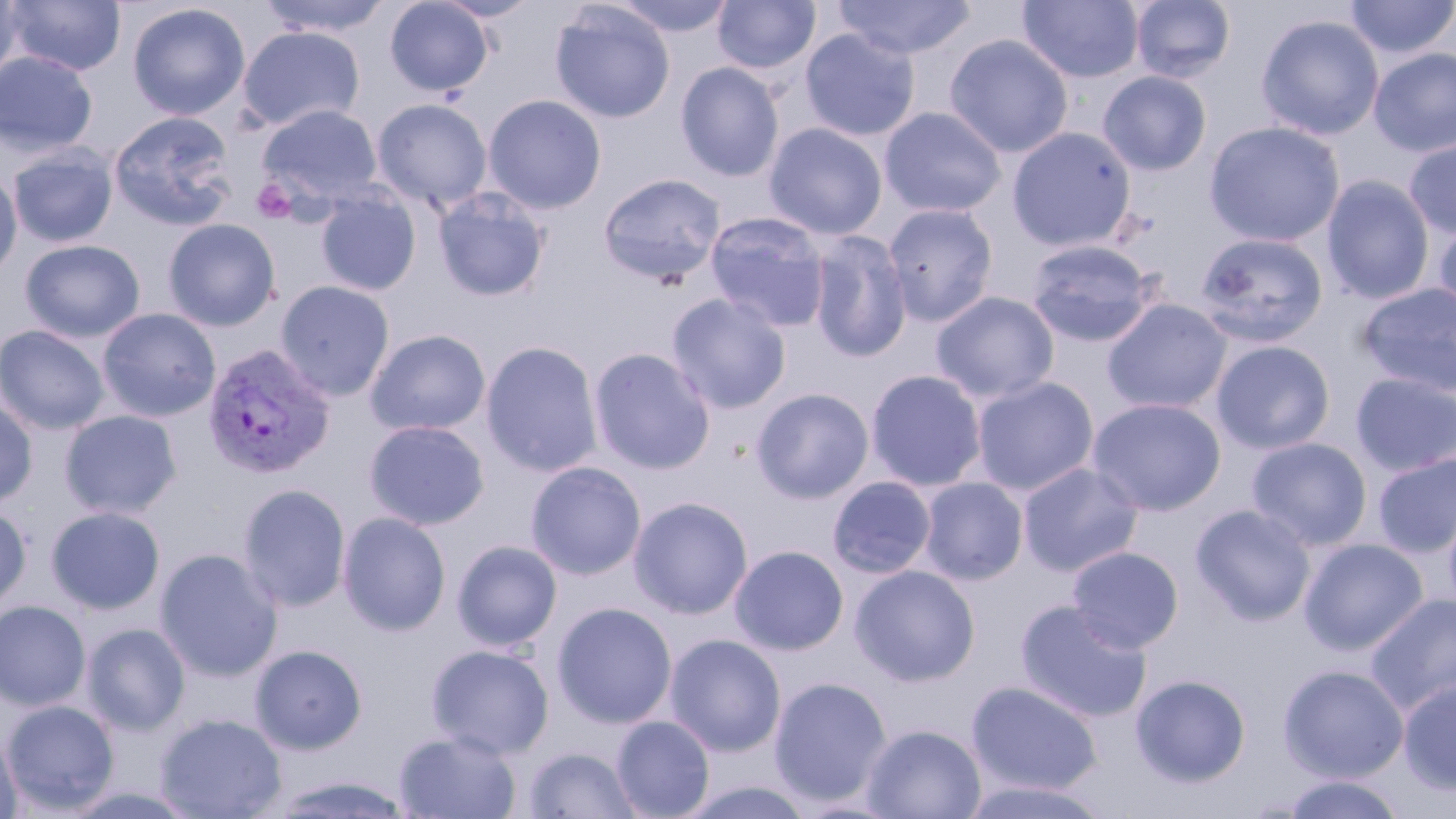

Approximate bounding boxes as (x1, y1, x2, y2) in pixels. Plasmodium vivax-infected red blood cell locations: (202, 344, 335, 478). Uninfected red blood cell locations: (0, 0, 24, 89), (4, 0, 126, 77), (256, 0, 394, 37), (384, 0, 494, 97), (432, 0, 542, 21), (611, 0, 735, 37), (712, 0, 821, 75), (829, 0, 977, 61), (1130, 0, 1235, 84), (1343, 0, 1456, 60), (1017, 1, 1145, 84), (126, 3, 250, 121), (550, 3, 675, 124), (1255, 14, 1385, 140), (238, 26, 365, 132), (799, 27, 921, 141), (944, 34, 1073, 158), (1368, 47, 1456, 157), (0, 51, 98, 158), (676, 62, 785, 182), (1097, 70, 1212, 176), (483, 94, 607, 214), (371, 98, 493, 212), (258, 104, 383, 207), (879, 106, 1007, 218), (108, 111, 237, 231), (1204, 121, 1345, 247), (764, 122, 887, 240), (1008, 127, 1136, 251), (1403, 137, 1456, 239), (7, 146, 117, 248), (0, 166, 23, 284), (597, 172, 726, 287), (1322, 174, 1435, 305), (432, 189, 551, 302), (316, 191, 421, 296), (882, 203, 999, 326), (705, 213, 832, 332), (1432, 215, 1456, 327), (163, 218, 281, 331), (808, 231, 913, 362), (1195, 232, 1328, 347), (19, 239, 145, 342), (1024, 239, 1159, 347), (275, 280, 395, 400), (1358, 282, 1456, 398), (931, 291, 1060, 403), (667, 293, 792, 414), (1102, 299, 1232, 413), (97, 308, 221, 422), (0, 324, 110, 435), (365, 329, 491, 436), (1212, 339, 1336, 454), (481, 341, 603, 477), (588, 347, 716, 475), (866, 369, 988, 492), (1351, 372, 1456, 475), (971, 376, 1099, 495), (751, 387, 875, 504), (0, 397, 38, 509), (1088, 397, 1226, 515), (60, 409, 182, 519), (363, 420, 490, 530), (354, 423, 472, 632), (1246, 437, 1372, 551), (1373, 452, 1456, 557), (525, 461, 646, 580), (1018, 462, 1143, 576), (827, 475, 937, 579), (918, 477, 1028, 585), (238, 483, 352, 612), (629, 496, 753, 619), (0, 503, 31, 612), (1190, 504, 1316, 626), (46, 506, 166, 615), (337, 512, 451, 635), (1299, 538, 1428, 655), (452, 540, 562, 650), (729, 545, 849, 655), (1067, 546, 1184, 653), (154, 548, 283, 681), (850, 565, 980, 687), (1364, 592, 1456, 717), (1015, 599, 1152, 723), (0, 601, 91, 711), (552, 602, 677, 729), (82, 623, 191, 735), (665, 633, 787, 757), (249, 644, 368, 754), (426, 644, 554, 758), (1277, 663, 1410, 782), (1130, 674, 1252, 787), (769, 677, 892, 806), (1398, 677, 1456, 796), (966, 681, 1103, 795), (2, 699, 120, 814), (155, 713, 287, 819), (611, 716, 715, 819), (861, 724, 986, 819), (1, 729, 23, 819), (393, 729, 522, 819), (523, 746, 643, 818), (264, 773, 417, 818), (1277, 774, 1409, 818), (957, 778, 1114, 819), (677, 779, 818, 819), (56, 785, 205, 819). Platelet locations: (252, 178, 297, 224). Slide-level diagnosis: Plasmodium vivax. May-Grünwald-Giemsa stain. Image is 1456×819 pixels. 1000x magnification. Thin blood smear. Light microscopy. Single field of view.